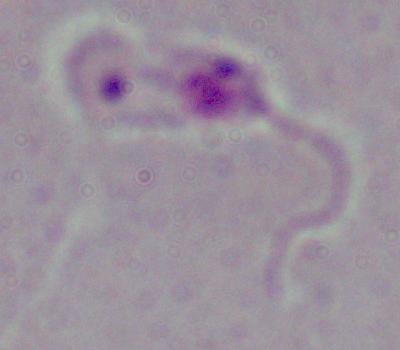

Summary:
  - Magnification: 1000x
  - Identification: Leishmania
  - Modality: micrograph